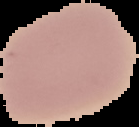
From a thin blood smear. The area outside the segmented cell region is set to black. Malaria status: uninfected. Image is 139×127 pixels.